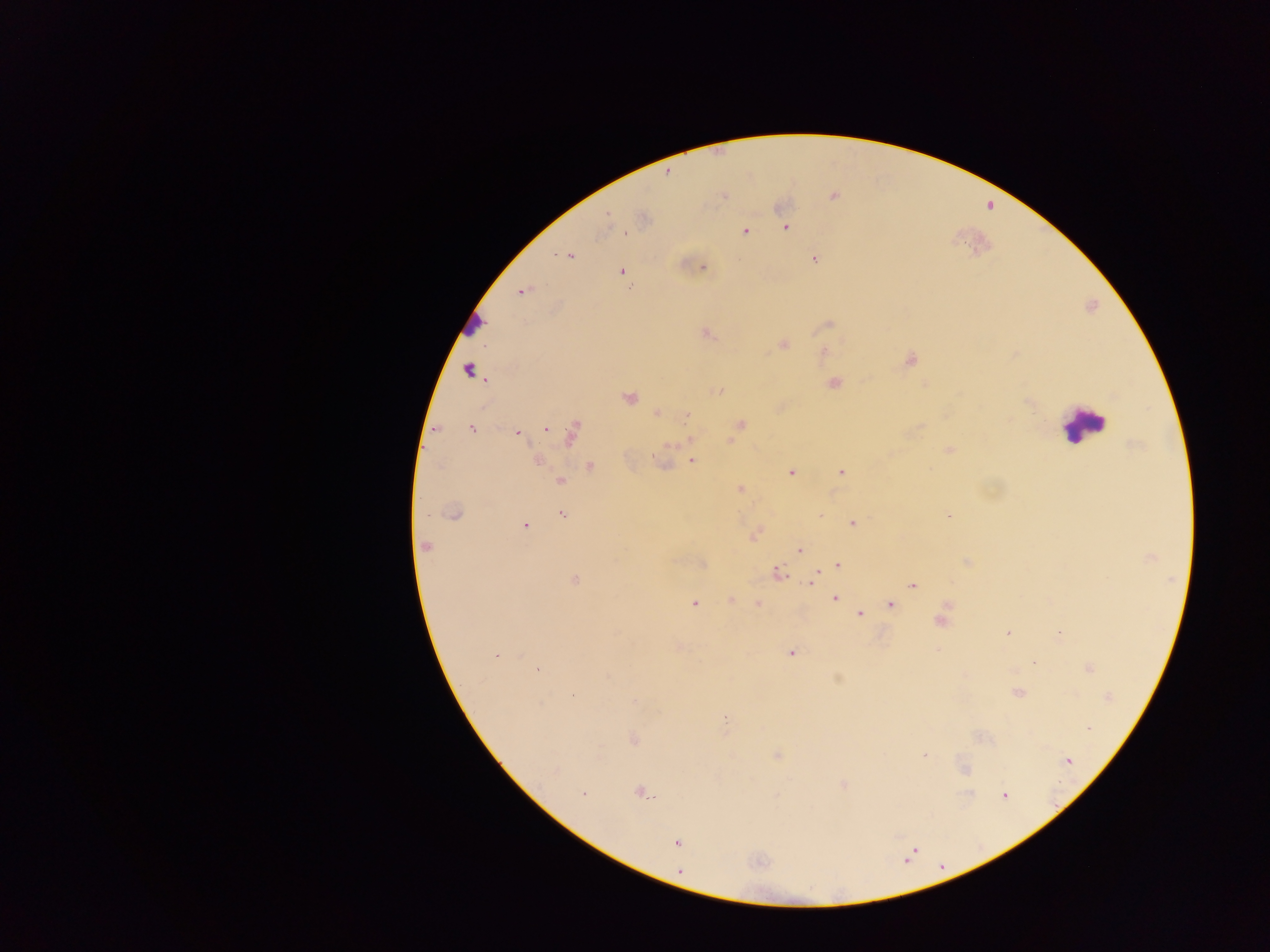
Approximate centers as (x, y) in pixels. Malaria parasite locations: (724, 196), (607, 217), (785, 228), (745, 231), (626, 232), (570, 256), (815, 259), (703, 267), (622, 271), (630, 288), (522, 291), (829, 325), (707, 333), (783, 344), (910, 359), (468, 370), (834, 383), (719, 390), (629, 397), (657, 413), (687, 415), (741, 425), (546, 428), (471, 429), (517, 433), (571, 433), (692, 439), (950, 450), (537, 461), (693, 461), (591, 467), (841, 472), (791, 473), (560, 481), (740, 489), (453, 513), (562, 514), (949, 516), (853, 523), (525, 525), (425, 546), (800, 550), (837, 564), (778, 572), (814, 575), (574, 580), (812, 581), (913, 586), (835, 597), (731, 601), (694, 604), (890, 604), (758, 605), (860, 614), (940, 621), (1007, 633), (1060, 635), (792, 652), (497, 655), (1034, 663), (1089, 668), (538, 669), (1018, 693), (1108, 697), (725, 718), (1088, 728), (633, 738), (924, 754), (1069, 761), (965, 769), (556, 770), (843, 785), (640, 793), (582, 794), (1005, 795), (677, 843). Leukocyte locations: (473, 325), (1084, 425). Mobile-phone photograph taken through the microscope. Collected in Ghana. Image is 1270×952 pixels. Thick blood film. One field of view.